Assess this cell for malaria.
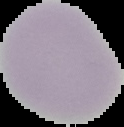
It is uninfected.

From a thin blood film. Segmented cell region on a black background. Image is 124×127 pixels.